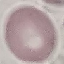
Summary:
  - Result: no malaria parasites seen
  - Image type: cell patch, automatically extracted from a larger field of view and resized to 64 × 64 pixels
  - Capture: smartphone camera at the microscope eyepiece
  - Stain: Giemsa
  - Preparation: thin blood film